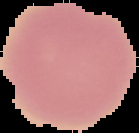
Image is 139×133 pixels. Result: no malaria parasites seen. From a thin blood smear. Cell region segmented out of the field of view; the surrounding area is masked to black.